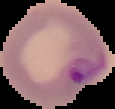

Summary:
  - Preparation: thin blood film
  - Image type: segmented cell region with the area outside set to black
  - Result: Plasmodium parasites identified
  - Image size: 115×109 pixels